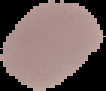

Summary:
  - Image size: 106×91 pixels
  - Malaria status: uninfected
  - Image type: segmented cell region with the area outside set to black
  - Preparation: thin blood film